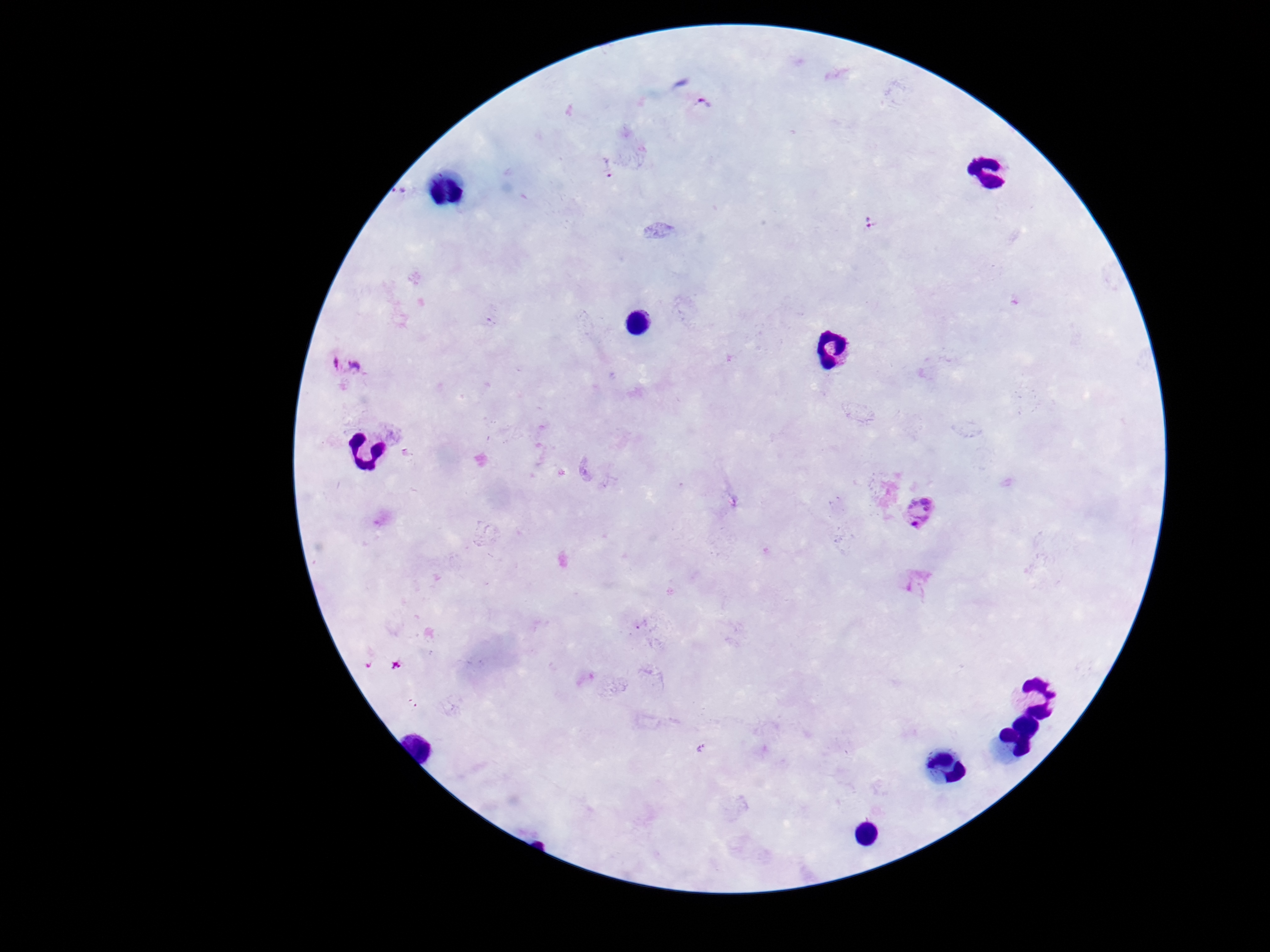

Approximate centers as [x, y] in pixels. Plasmodium parasite locations: [701, 109], [608, 167], [872, 223], [347, 366], [920, 513], [917, 580], [701, 748]. Image is 1270×952 pixels. Patient malaria status: positive. One field from this slide. Giemsa-stained preparation. Thick blood smear. 100x magnification. Photographed through the microscope eyepiece with a smartphone camera.